Describe the morphology of the red blood cells.
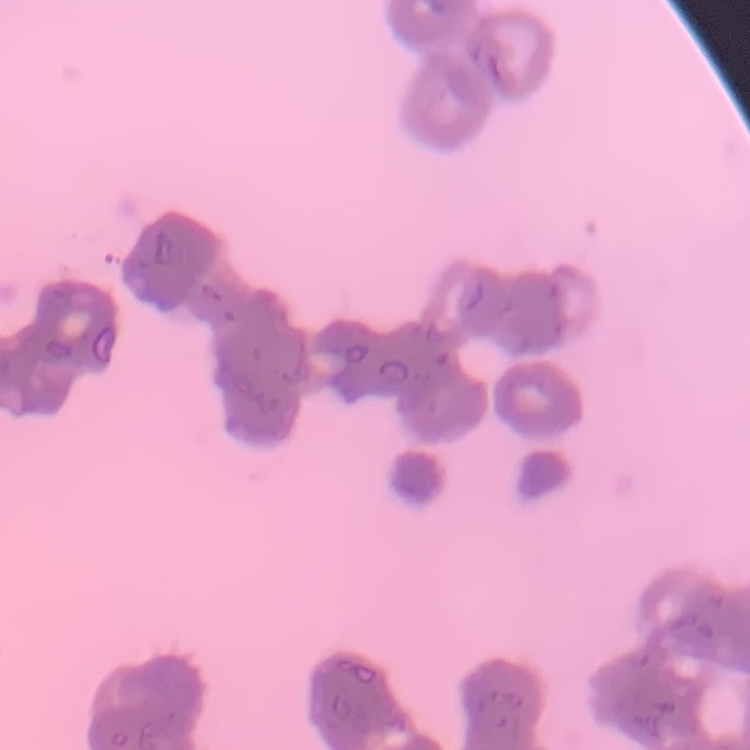
Rouleaux formation.

Field's or Giemsa stain. One tile cut from a larger photomicrograph. Thin peripheral smear.